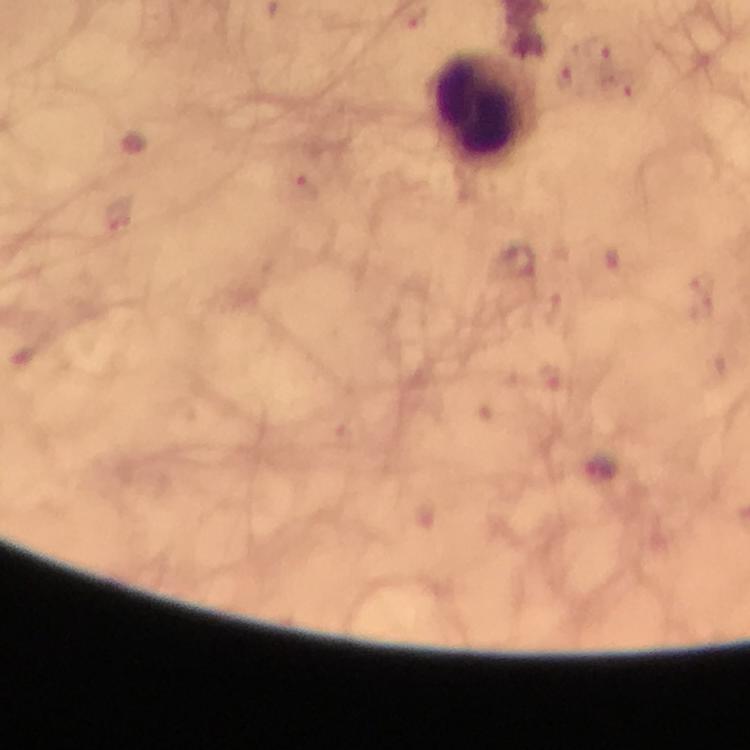

Approximate centers as [x, y] in pixels.
Summary:
  - Leukocyte locations: [487, 108]
  - Malaria parasite locations: [595, 50], [564, 79], [618, 88], [304, 188], [119, 216], [517, 262], [548, 377]
  - Magnification: 100x
  - Capture: smartphone mounted on the microscope
  - Image size: 750×750 pixels
  - Stain: Giemsa
  - Context: from a diagnostic examination for malaria
  - Cropped from: a single field of view
  - Immersion oil: used
  - Preparation: thick blood film